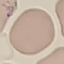
{
  "malaria_status": "uninfected",
  "image_type": "automatically extracted cell patch, resized to 64 × 64 pixels",
  "preparation": "thin smear",
  "stain": "Giemsa",
  "capture": "smartphone camera at the microscope eyepiece"
}